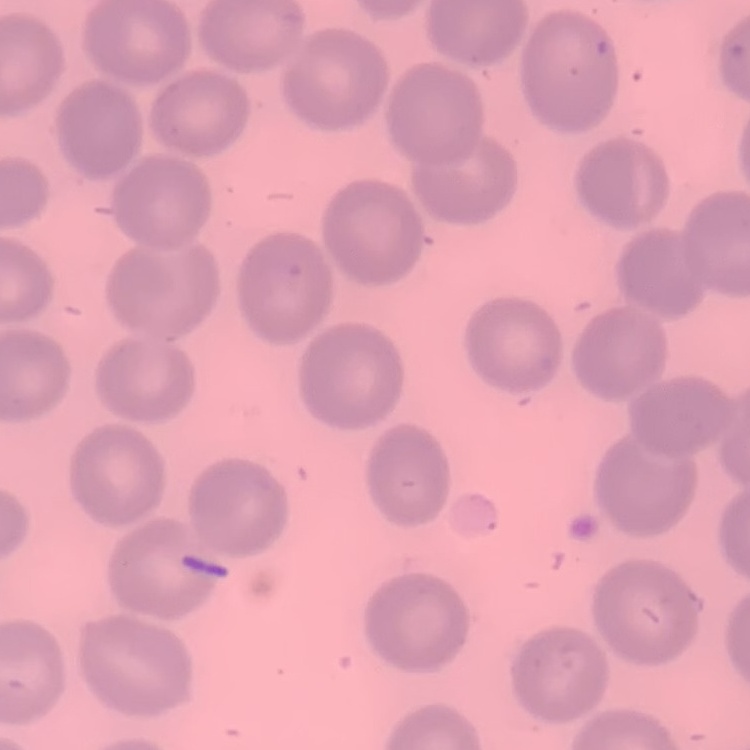
The erythrocytes exhibit no rouleaux formation. Field's or Giemsa stain. One tile cut from a larger photomicrograph. Thin blood film.